Comment on the morphology of the erythrocytes.
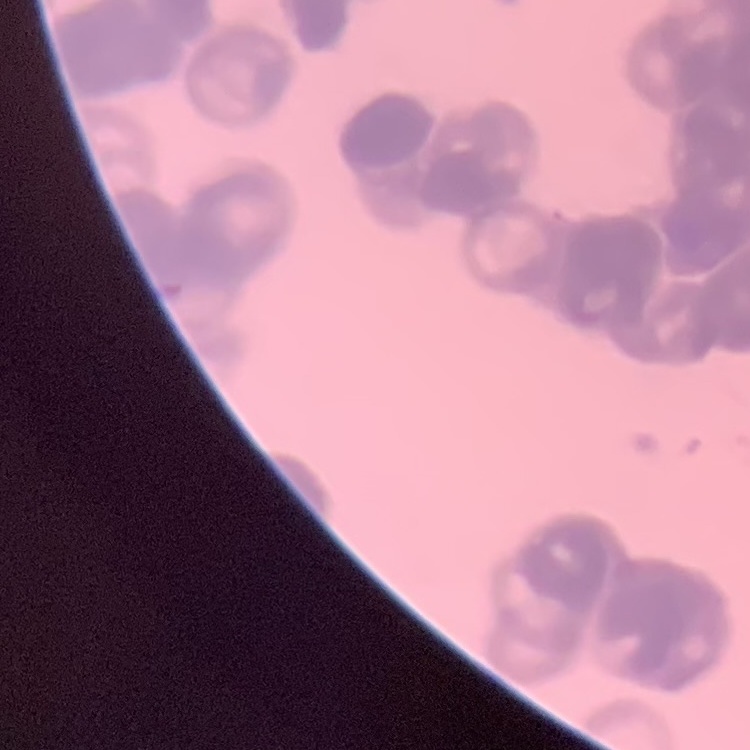
Rouleaux formation.

One tile cut from a larger photomicrograph. Field's or Giemsa stain. Thin peripheral smear.